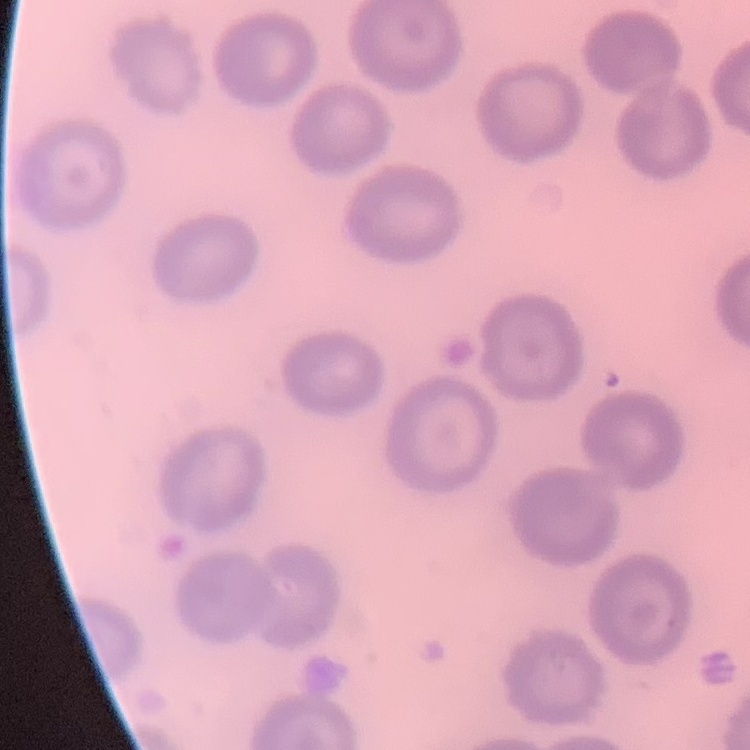 The erythrocytes exhibit no rouleaux formation. Thin blood smear. Stained with either Field's or Giemsa. One tile cut from a larger photomicrograph.